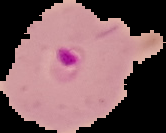
image_type: cell region segmented out of the field of view; surrounding area masked to black
preparation: thin blood smear
malaria_status: parasitized
image_size: 166×133 pixels